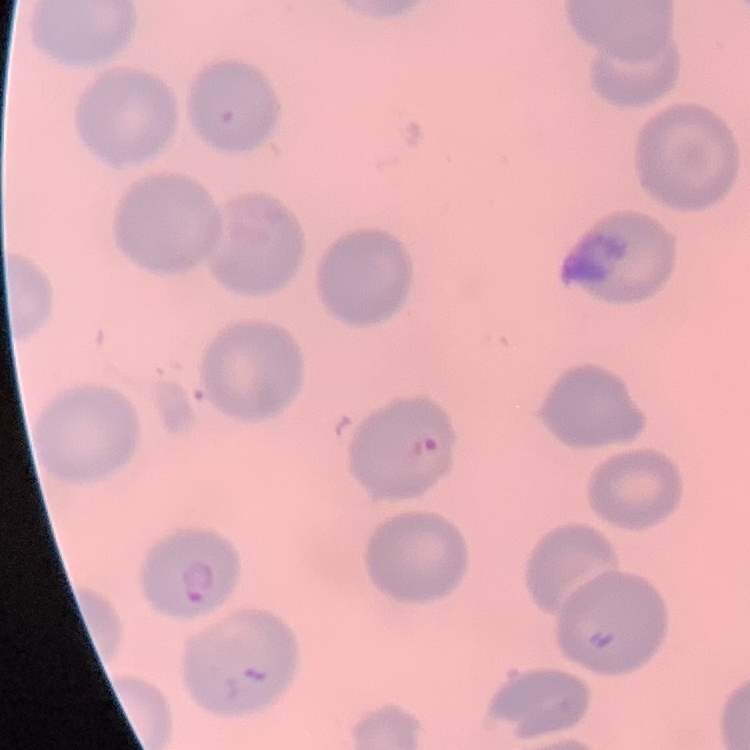

Summary:
  - Red blood cell morphology: no rouleaux formation
  - Stain: Field's or Giemsa
  - Image type: one tile cut from a larger photomicrograph
  - Preparation: thin blood film